State which cell type is depicted.
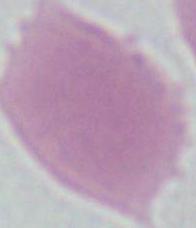

This is an erythrocyte.

Summary:
  - Modality: micrograph
  - Magnification: 1000x